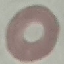
Summary:
  - Result: negative for malaria parasites
  - Stain: Giemsa
  - Capture: smartphone camera at the microscope eyepiece
  - Image type: automatically extracted cell patch, resized to 64 × 64 pixels
  - Preparation: thin blood smear